Describe the morphology of the erythrocytes.
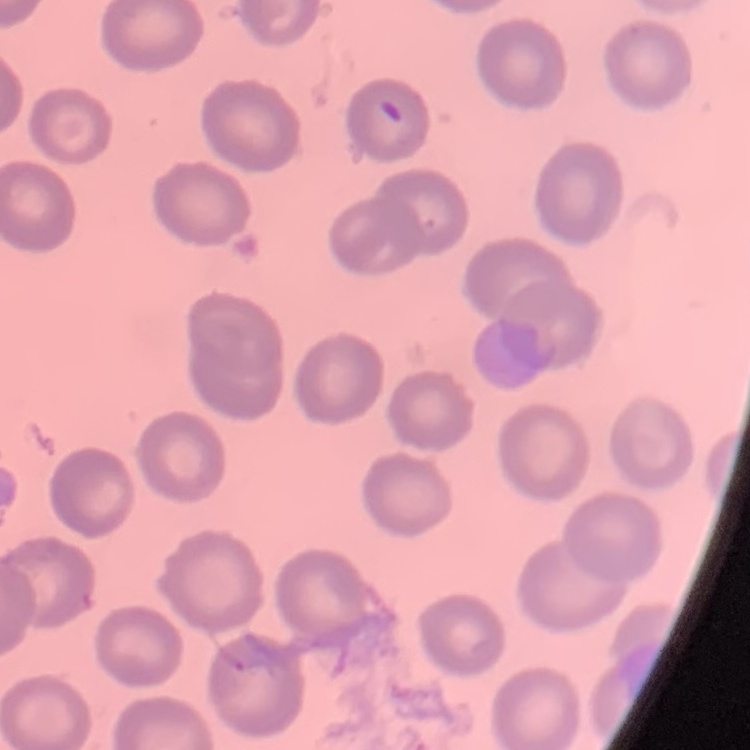

They show no rouleaux formation.

One tile cut from a larger photomicrograph. Stained with either Field's or Giemsa. Thin blood smear.